Report the malaria status of this cell.
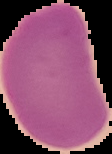
It is uninfected.

From a thin blood smear. Image is 112×154 pixels. Segmented cell region on a black background.